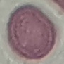

Summary:
  - Malaria status: uninfected
  - Image type: cell patch, automatically extracted from a larger field of view and resized to 64 × 64 pixels
  - Stain: Giemsa
  - Capture: smartphone through the microscope eyepiece
  - Preparation: thin blood smear